Identify the parasite.
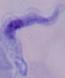
This is a trypanosome.

Photomicrograph. Captured at 1000x magnification.